Classify this cell by malaria status.
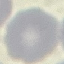
Uninfected.

Summary:
  - Preparation: thin blood film
  - Stain: Giemsa
  - Capture: smartphone camera at the microscope eyepiece
  - Image type: automatically extracted cell patch, resized to 64 × 64 pixels